Locate and identify every blood parasite.
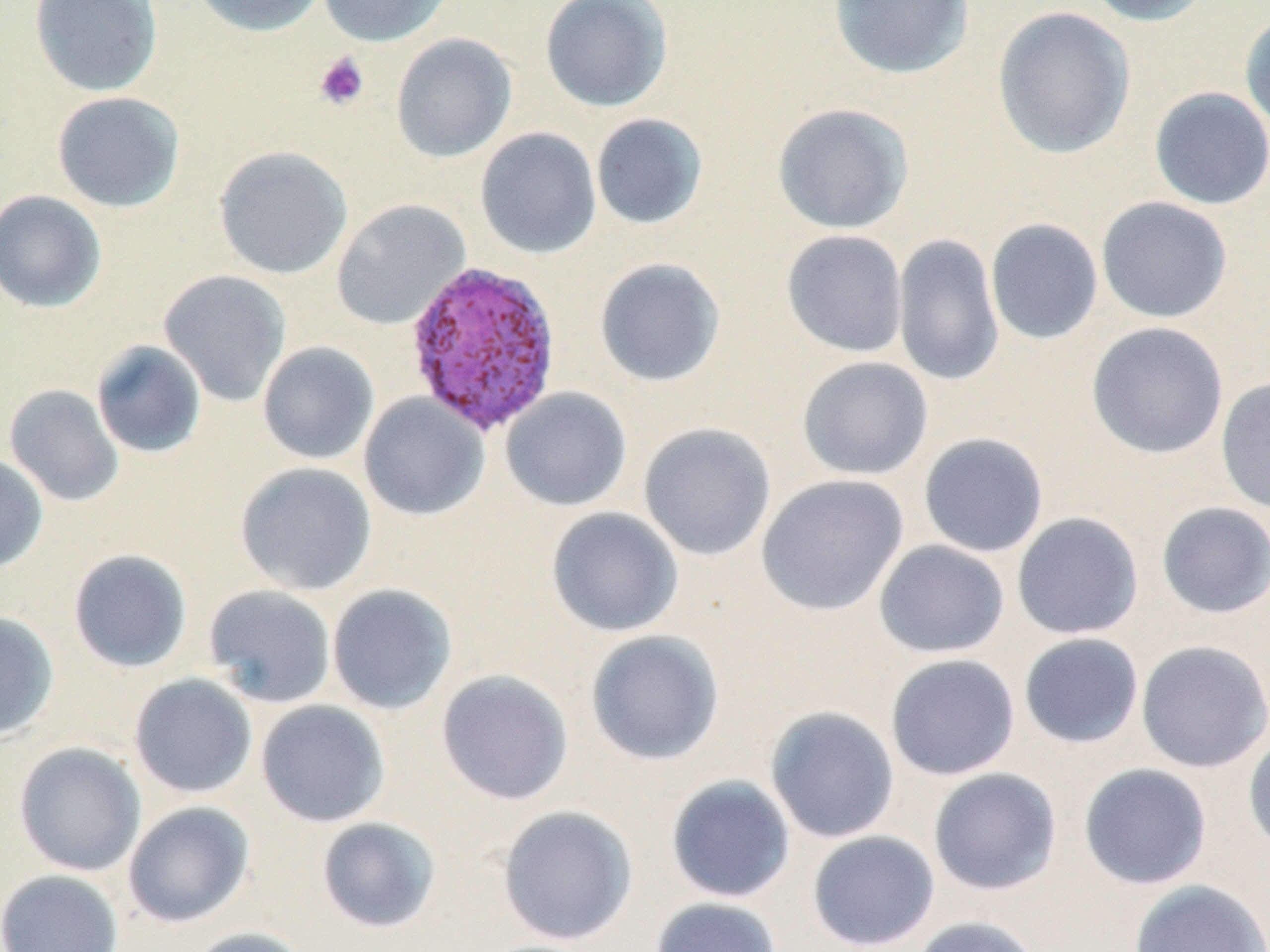
Approximate bounding boxes as (x1,y1)-(x2,y2) corner pairs in pixels.
Plasmodium vivax-infected red blood cells: (403,260)-(563,436).
No Plasmodium falciparum, Plasmodium ovale, Plasmodium malariae, Babesia divergens, or Trypanosoma brucei observed.

Summary:
  - Uninfected red blood cell locations: (29,0)-(163,97), (191,0)-(327,37), (317,0)-(454,47), (540,0)-(673,112), (828,0)-(975,80), (1081,0)-(1215,26), (992,6)-(1137,159), (1239,10)-(1270,136), (390,33)-(518,162), (1149,87)-(1270,209), (51,91)-(185,213), (771,103)-(914,235), (590,113)-(708,230), (475,127)-(601,259), (213,145)-(353,280), (0,189)-(107,313), (1096,196)-(1233,323), (330,199)-(470,331), (984,218)-(1104,345), (781,229)-(909,358), (892,233)-(1005,387), (594,257)-(727,387), (159,269)-(292,407), (1085,321)-(1229,459), (91,340)-(207,458), (257,341)-(379,465), (796,356)-(933,480), (1216,376)-(1270,516), (4,384)-(124,507), (500,386)-(632,511), (359,393)-(489,521), (637,422)-(776,561), (917,432)-(1049,558), (0,452)-(49,575), (235,461)-(377,596), (756,474)-(908,616), (1156,501)-(1270,619), (545,507)-(684,637), (1011,512)-(1144,640), (874,540)-(1009,658), (68,548)-(192,673), (203,584)-(337,708), (326,584)-(457,715), (0,611)-(59,740), (584,629)-(725,766), (1018,632)-(1144,749), (1135,640)-(1270,773), (884,653)-(1020,781), (436,669)-(574,805), (129,673)-(258,798), (255,700)-(390,827), (765,705)-(900,844), (1243,732)-(1270,857), (13,741)-(146,876), (1078,763)-(1212,890), (927,768)-(1062,896), (665,775)-(796,903), (123,801)-(255,927), (496,805)-(638,946), (316,816)-(442,934), (806,830)-(940,951), (0,869)-(123,952), (1128,880)-(1269,952), (649,896)-(782,952), (910,916)-(1042,952), (185,926)-(312,952)
  - Platelet locations: (313,51)-(370,110)
  - Slide-level diagnosis: Plasmodium vivax
  - Field of view: single
  - Modality: light microscopy
  - Preparation: thin blood film
  - Image size: 1270×952 pixels
  - Magnification: 1000x
  - Stain: May-Grünwald-Giemsa